State the preparation type.
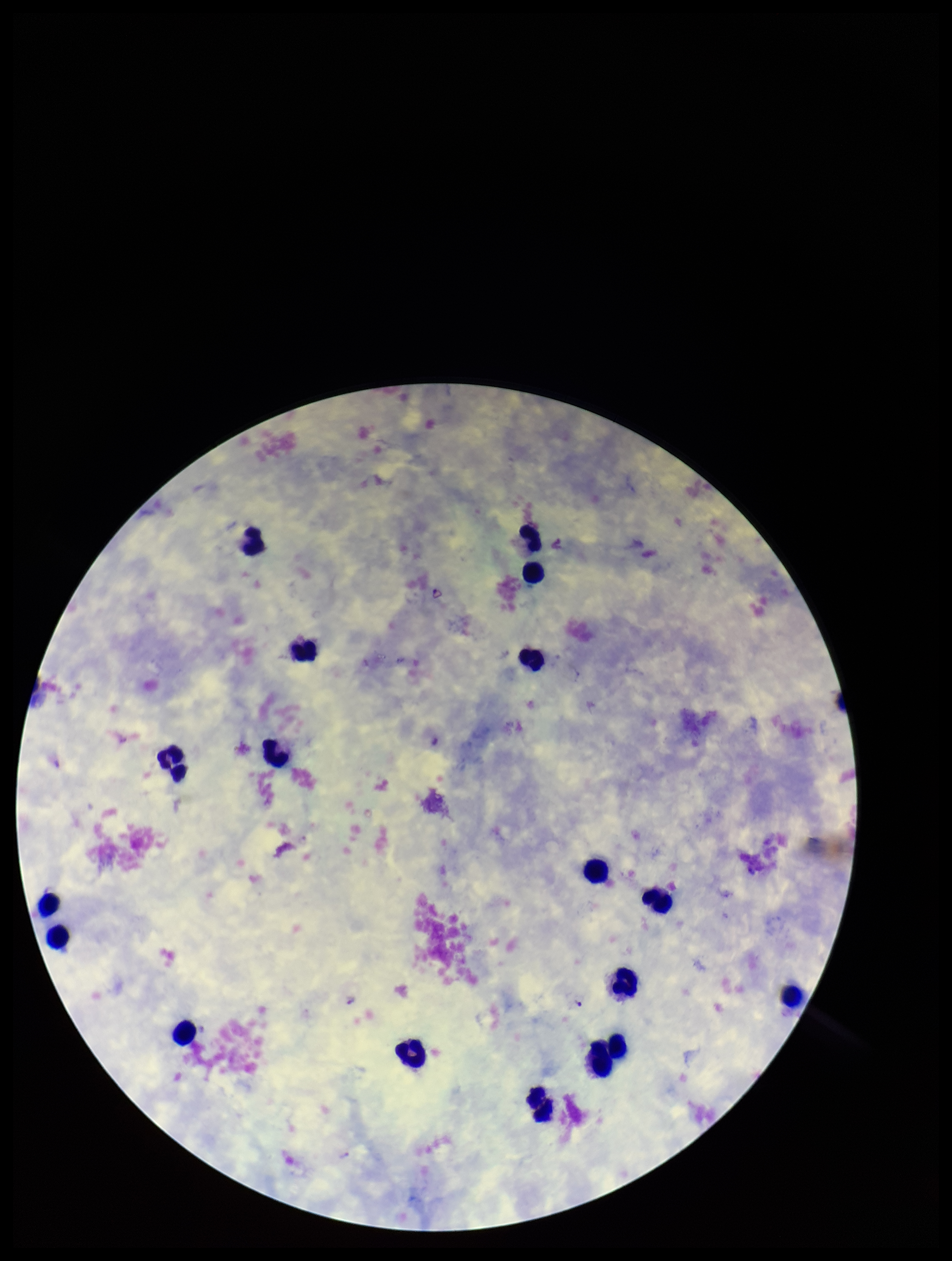
Thick.

patient_malaria_status: positive
stain: Giemsa
parasite_count: 3
capture: smartphone photograph through the microscope eyepiece
plasmodium_parasites: seen
leukocyte_count: 18
image_size: 952×1261 pixels
field_of_view: one from this slide
species_reported_for_this_patient: Plasmodium vivax